Report the malaria status of this cell.
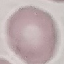

It is uninfected.

preparation: thin blood smear
stain: Giemsa
image_type: cell patch, automatically extracted from a larger field of view and resized to 64 × 64 pixels
capture: smartphone through the microscope eyepiece